Classify this cell by malaria status.
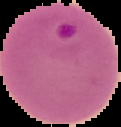
It is parasitized.

image size = 121×127 pixels
image type = cell region segmented out of the field of view; surrounding area masked to black
preparation = thin blood film